Classify this cell by malaria status.
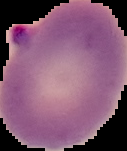
Parasitized.

Summary:
  - Preparation: thin blood film
  - Image size: 127×151 pixels
  - Image type: cell region segmented out of the field of view; surrounding area masked to black